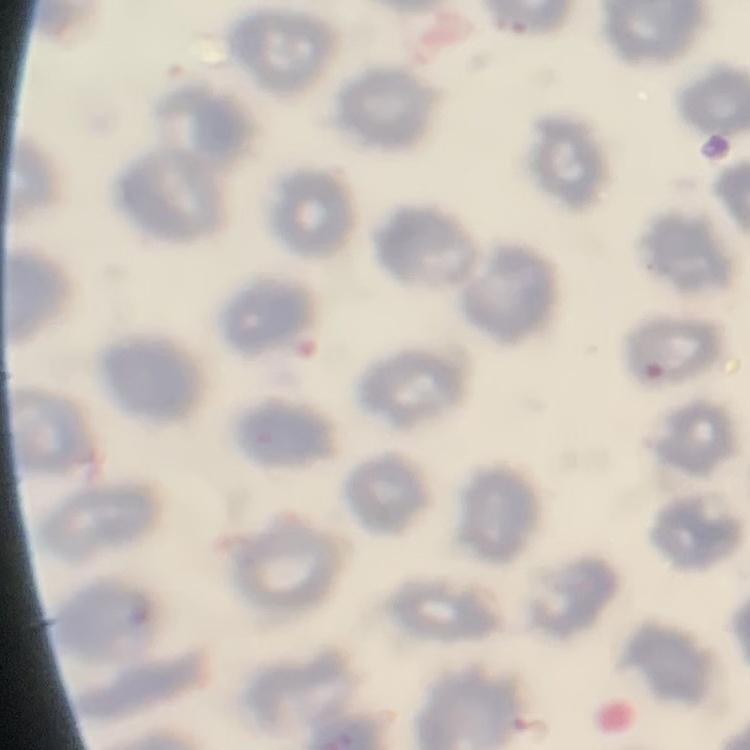
erythrocyte morphology = no rouleaux formation
image type = square crop of a larger photomicrograph
preparation = thin peripheral smear
stain = Field's or Giemsa